Mark where platelets are.
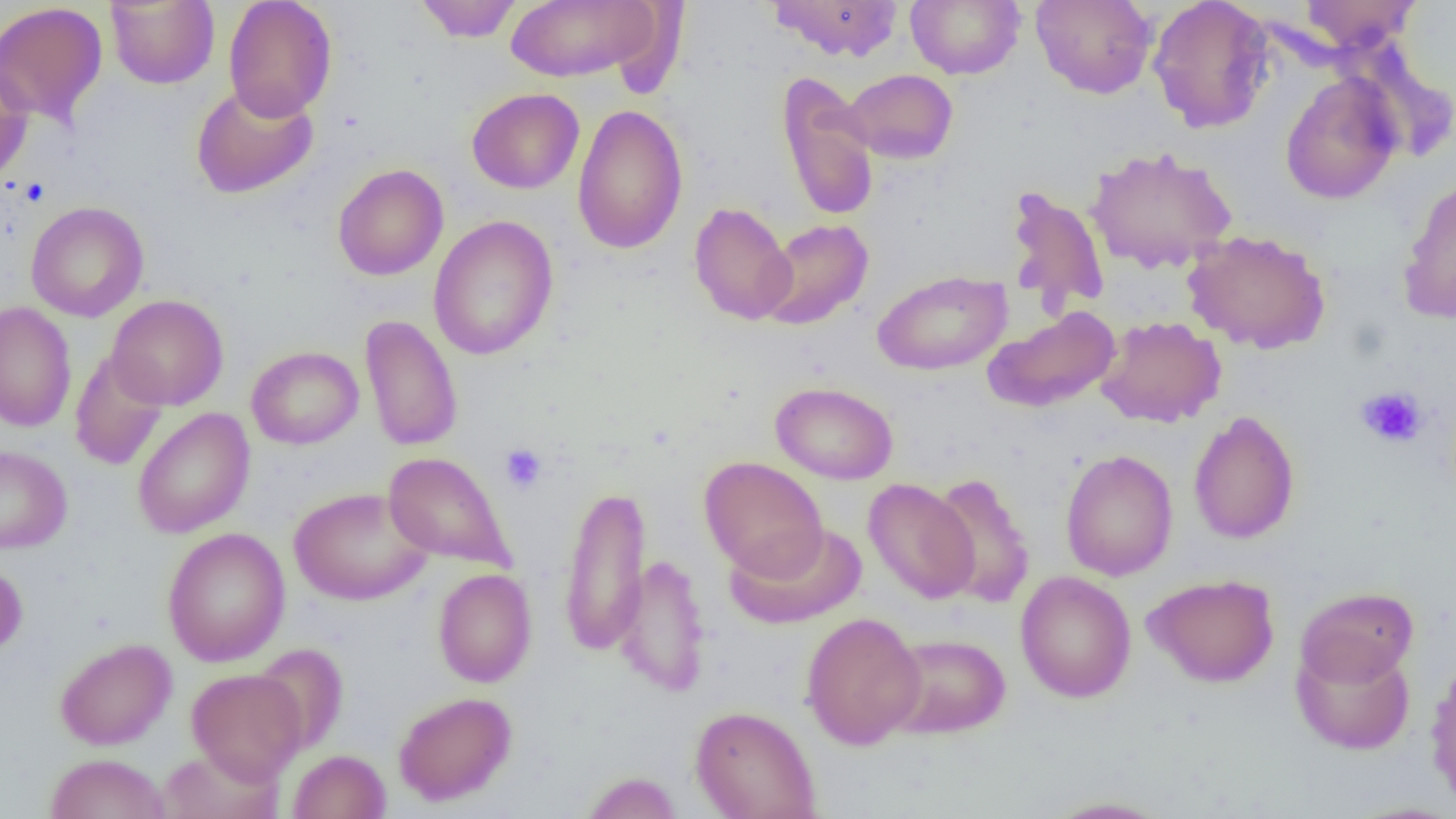
Approximate bounding boxes as named x1/y1/x2/y2 corners in pixels.
Platelets: (x1=15, y1=178, x2=48, y2=206), (x1=1355, y1=385, x2=1428, y2=449), (x1=499, y1=443, x2=547, y2=494).

Uninfected red blood cell locations: (x1=105, y1=0, x2=219, y2=89), (x1=223, y1=0, x2=338, y2=121), (x1=414, y1=0, x2=524, y2=42), (x1=504, y1=0, x2=662, y2=83), (x1=767, y1=0, x2=904, y2=62), (x1=906, y1=0, x2=1025, y2=79), (x1=1031, y1=0, x2=1157, y2=99), (x1=1146, y1=0, x2=1275, y2=133), (x1=1297, y1=0, x2=1421, y2=52), (x1=0, y1=2, x2=108, y2=127), (x1=0, y1=61, x2=34, y2=187), (x1=842, y1=68, x2=958, y2=163), (x1=776, y1=72, x2=879, y2=222), (x1=1280, y1=73, x2=1401, y2=205), (x1=191, y1=82, x2=318, y2=199), (x1=466, y1=87, x2=584, y2=194), (x1=572, y1=103, x2=689, y2=255), (x1=1085, y1=146, x2=1237, y2=274), (x1=332, y1=163, x2=448, y2=281), (x1=1398, y1=176, x2=1456, y2=325), (x1=1005, y1=185, x2=1110, y2=315), (x1=25, y1=201, x2=149, y2=322), (x1=688, y1=201, x2=797, y2=325), (x1=428, y1=215, x2=559, y2=360), (x1=758, y1=218, x2=873, y2=331), (x1=1183, y1=230, x2=1331, y2=354), (x1=873, y1=270, x2=1011, y2=375), (x1=106, y1=295, x2=228, y2=410), (x1=0, y1=302, x2=76, y2=432), (x1=984, y1=306, x2=1120, y2=412), (x1=360, y1=315, x2=463, y2=452), (x1=1095, y1=316, x2=1226, y2=427), (x1=246, y1=345, x2=363, y2=449), (x1=69, y1=350, x2=169, y2=471), (x1=770, y1=381, x2=898, y2=485), (x1=132, y1=407, x2=255, y2=538), (x1=1188, y1=410, x2=1300, y2=545), (x1=0, y1=445, x2=72, y2=553), (x1=1060, y1=449, x2=1178, y2=581), (x1=383, y1=452, x2=514, y2=571), (x1=699, y1=456, x2=828, y2=579), (x1=929, y1=472, x2=1035, y2=607), (x1=863, y1=477, x2=979, y2=604), (x1=558, y1=482, x2=652, y2=657), (x1=289, y1=486, x2=432, y2=605), (x1=724, y1=522, x2=867, y2=629), (x1=162, y1=527, x2=290, y2=667), (x1=614, y1=553, x2=712, y2=698), (x1=0, y1=560, x2=28, y2=659), (x1=433, y1=568, x2=537, y2=687), (x1=1015, y1=571, x2=1137, y2=703), (x1=1142, y1=574, x2=1280, y2=688), (x1=1296, y1=586, x2=1419, y2=688), (x1=800, y1=611, x2=925, y2=750), (x1=883, y1=633, x2=1011, y2=739), (x1=54, y1=638, x2=176, y2=750), (x1=1291, y1=638, x2=1416, y2=755), (x1=252, y1=644, x2=348, y2=755), (x1=1425, y1=659, x2=1456, y2=808), (x1=186, y1=668, x2=307, y2=783), (x1=393, y1=691, x2=517, y2=806), (x1=690, y1=705, x2=821, y2=819), (x1=160, y1=745, x2=284, y2=818), (x1=288, y1=749, x2=391, y2=819), (x1=45, y1=753, x2=171, y2=819), (x1=580, y1=771, x2=683, y2=818), (x1=1042, y1=796, x2=1174, y2=818). Slide-level diagnosis: no evidence of blood parasites. Image is 1456×819 pixels. Captured at 1000x magnification. Thin blood smear. One field of a larger specimen. Optical microscopy.